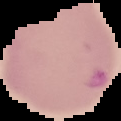

result = Plasmodium parasites detected
image type = segmented cell region with the area outside set to black
preparation = thin blood film
image size = 121×121 pixels